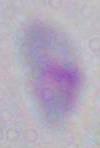

Summary:
  - Modality: photomicrograph
  - Identification: Toxoplasma gondii
  - Magnification: 1000x